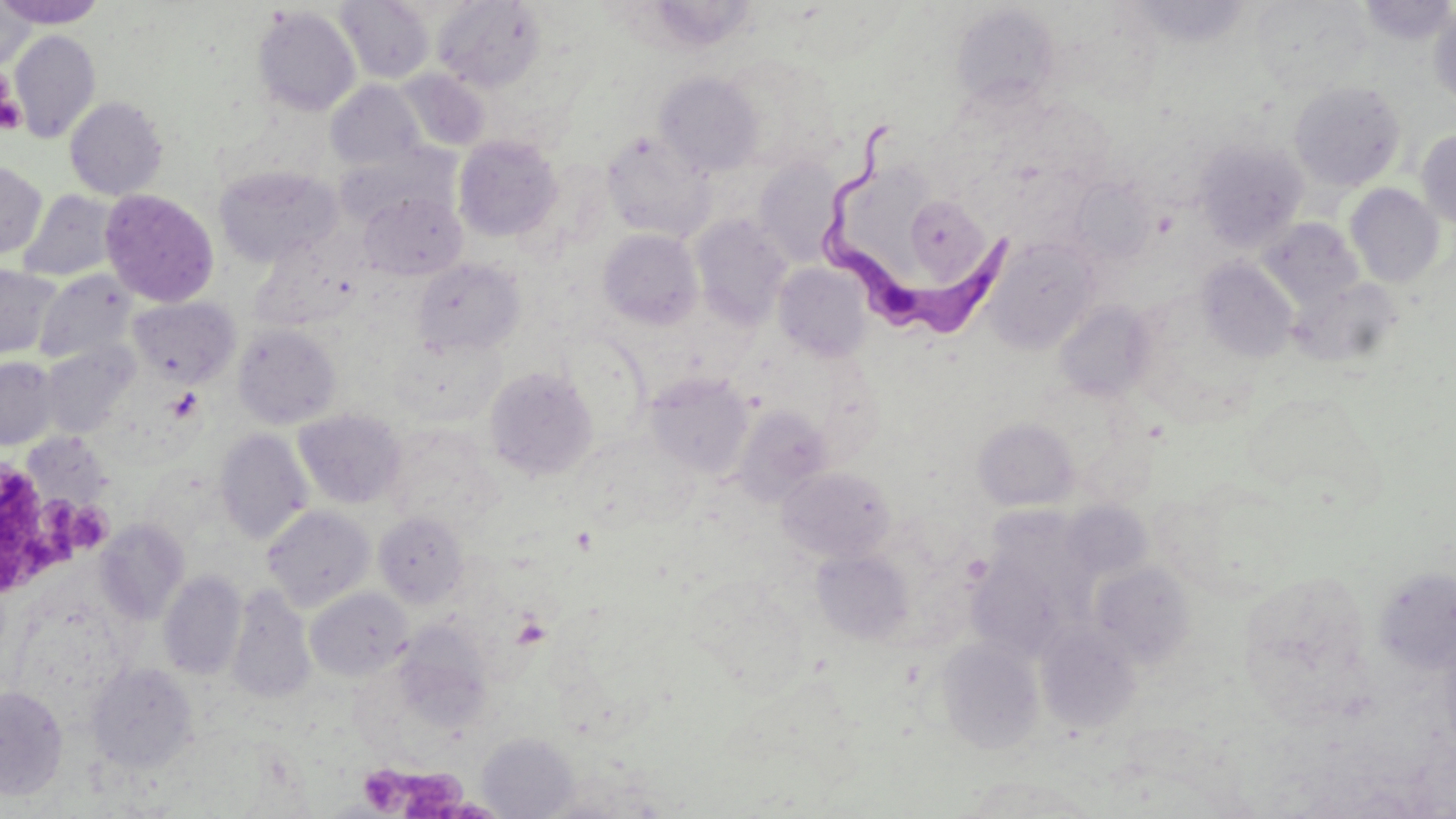

slide-level diagnosis = Trypanosoma brucei
preparation = thin blood smear
Trypanosoma brucei locations = approximate bounding boxes as (x1, y1, x2, y2) in pixels: (816, 122, 1014, 337)
stain = May-Grünwald-Giemsa
magnification = 1000x
image size = 1456×819 pixels
platelet locations = approximate bounding boxes as (x1, y1, x2, y2) in pixels: (1, 89, 25, 133), (167, 387, 204, 423), (0, 468, 48, 588), (37, 495, 82, 542), (72, 506, 111, 549), (361, 769, 406, 804), (405, 770, 469, 818)
uninfected red blood cell locations = approximate bounding boxes as (x1, y1, x2, y2) in pixels: (1, 0, 105, 28), (1356, 0, 1456, 45), (0, 1, 34, 70), (337, 1, 434, 84), (433, 1, 546, 93), (1129, 1, 1258, 49), (1250, 1, 1372, 95), (950, 4, 1062, 109), (253, 5, 361, 117), (1428, 6, 1456, 107), (9, 30, 101, 143), (716, 54, 841, 170), (396, 68, 491, 151), (654, 71, 763, 176), (325, 81, 426, 171), (1289, 81, 1406, 190), (65, 96, 167, 201), (1416, 129, 1456, 230), (601, 130, 715, 242), (453, 135, 563, 242), (1193, 138, 1309, 251), (338, 147, 454, 229), (753, 156, 845, 266), (0, 161, 47, 259), (214, 165, 340, 267), (1069, 177, 1155, 264), (1346, 184, 1445, 287), (100, 188, 219, 307), (19, 190, 120, 282), (359, 191, 467, 281), (904, 195, 990, 287), (690, 214, 792, 328), (1256, 217, 1363, 310), (598, 228, 703, 329), (251, 233, 363, 332), (984, 235, 1101, 352), (1197, 257, 1299, 362), (412, 258, 525, 356), (774, 262, 873, 362), (0, 265, 62, 359), (35, 270, 136, 365), (1291, 277, 1403, 369), (129, 296, 239, 386), (1054, 300, 1157, 402), (232, 324, 342, 430), (392, 334, 508, 426), (41, 344, 137, 438), (0, 357, 59, 449), (484, 365, 598, 480), (645, 372, 754, 479), (1246, 391, 1384, 509), (732, 406, 832, 504), (294, 409, 406, 509), (973, 417, 1080, 511), (383, 425, 503, 537), (28, 428, 107, 510), (215, 428, 313, 545), (777, 466, 895, 562), (1166, 483, 1303, 599), (262, 505, 376, 611), (373, 511, 469, 608), (95, 519, 190, 625), (967, 547, 1075, 663), (812, 549, 914, 644), (1089, 561, 1196, 667), (1374, 566, 1456, 674), (158, 570, 247, 680), (1238, 570, 1373, 717), (227, 585, 315, 705), (306, 587, 413, 681), (395, 623, 493, 726), (1036, 623, 1142, 733), (935, 636, 1045, 754), (86, 662, 198, 773), (0, 685, 68, 800), (477, 733, 578, 818), (959, 775, 1102, 818)
modality = optical microscopy
field of view = single